Describe the morphology of the erythrocytes.
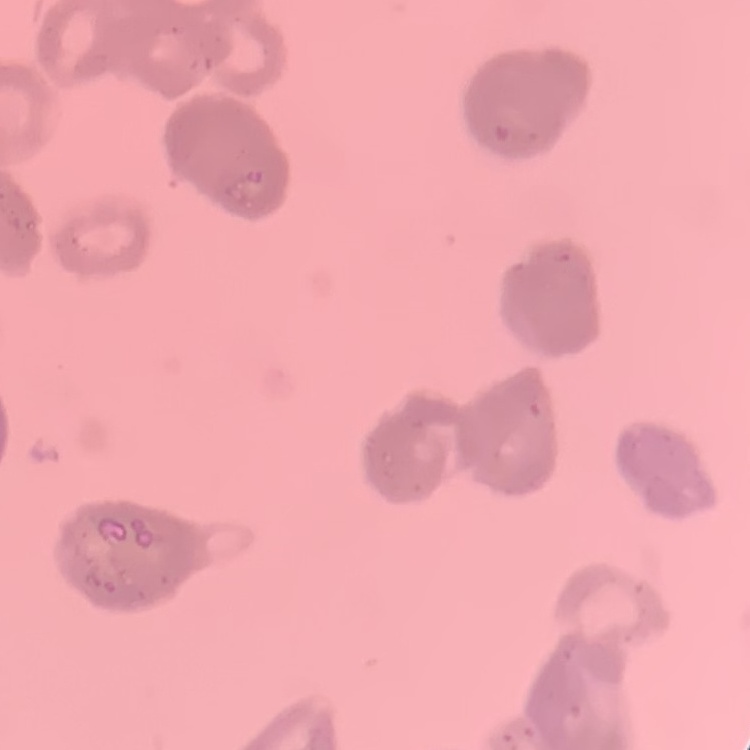
They show rouleaux formation.

Square crop of a larger photomicrograph. Stained with either Field's or Giemsa. Thin blood smear.